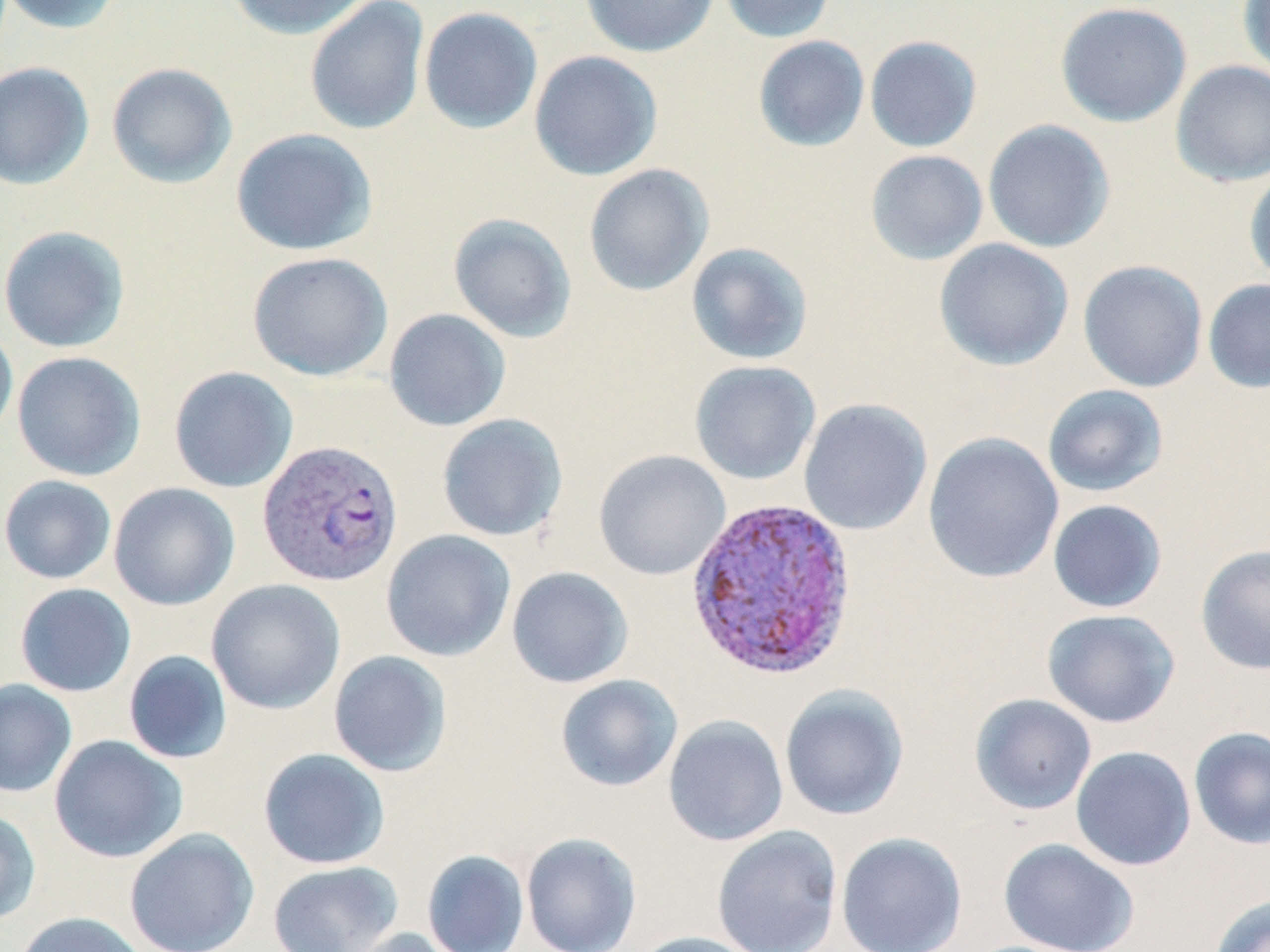 Approximate bounding boxes as (x1,y1)-(x2,y2) corner pairs in pixels. Plasmodium vivax-infected red blood cell locations: (257,438)-(403,587), (685,495)-(859,682). Uninfected red blood cell locations: (0,0)-(124,35), (225,0)-(373,40), (579,0)-(719,58), (719,0)-(837,43), (1238,0)-(1270,78), (304,1)-(430,135), (1055,1)-(1193,128), (418,6)-(543,134), (753,35)-(870,152), (864,35)-(983,153), (528,50)-(663,181), (1170,59)-(1270,187), (0,61)-(95,190), (106,62)-(237,189), (982,119)-(1115,253), (230,128)-(378,256), (865,149)-(988,266), (583,163)-(714,297), (1244,167)-(1270,288), (447,213)-(577,343), (0,224)-(131,353), (934,238)-(1075,371), (685,242)-(814,365), (247,251)-(394,381), (1078,259)-(1208,392), (1203,278)-(1270,394), (384,308)-(511,432), (0,322)-(18,443), (12,351)-(146,481), (689,360)-(822,485), (168,366)-(299,493), (1043,384)-(1168,497), (798,398)-(932,536), (437,413)-(569,541), (921,431)-(1064,584), (594,450)-(731,581), (0,475)-(117,584), (109,482)-(240,611), (1047,499)-(1167,613), (381,529)-(516,662), (1195,543)-(1270,675), (506,566)-(633,688), (206,579)-(346,714), (14,583)-(136,697), (1041,608)-(1181,728), (123,650)-(233,764), (328,650)-(452,777), (555,674)-(683,792), (0,679)-(78,799), (779,685)-(910,821), (970,693)-(1097,815), (662,715)-(789,846), (1188,726)-(1270,850), (49,734)-(188,863), (1070,746)-(1196,871), (257,748)-(391,870), (0,808)-(42,924), (711,825)-(843,952), (124,828)-(259,952), (521,832)-(642,952), (835,832)-(968,952), (998,838)-(1140,952), (422,849)-(529,952), (266,860)-(404,952), (1208,893)-(1270,952), (13,911)-(149,952), (338,927)-(464,952), (631,931)-(765,952). Slide-level diagnosis: Plasmodium vivax. Thin blood smear. Single field of view. Light microscopy. Image is 1270×952 pixels. Captured at 1000x magnification. May-Grünwald-Giemsa stain.